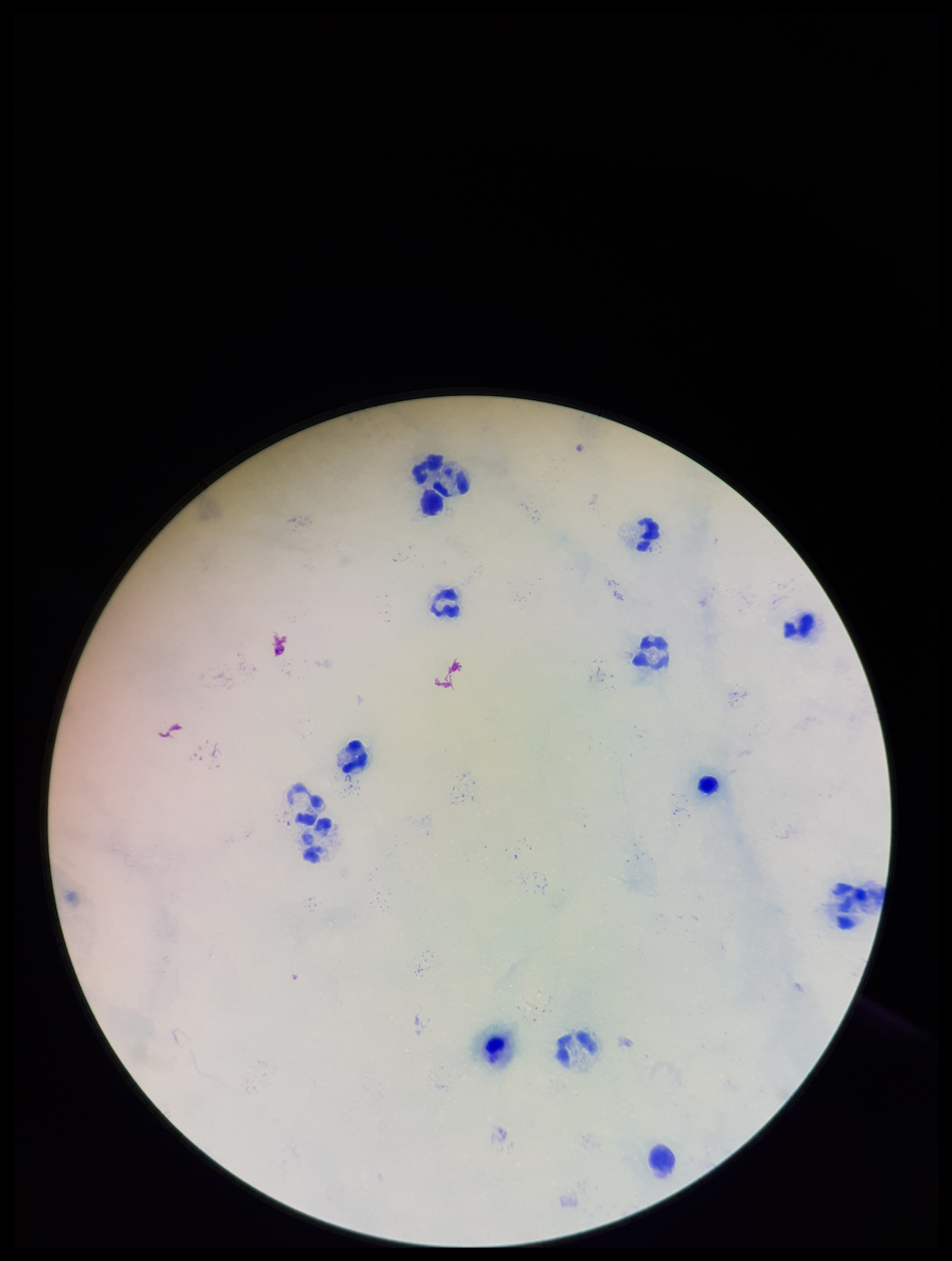
stain = Giemsa
patient malaria status = negative
image size = 952×1261 pixels
field of view = one from this slide
Plasmodium parasites = none identified
parasite count = 0
leukocyte count = 13
preparation = thick smear
capture = smartphone photograph through the microscope eyepiece